State which parasite is depicted.
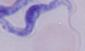

This is a trypanosome.

Summary:
  - Modality: photomicrograph
  - Magnification: 1000x